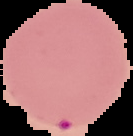
Summary:
  - Result: negative for Plasmodium parasites
  - Preparation: thin blood film
  - Image type: cell region segmented out of the field of view; surrounding area masked to black
  - Image size: 133×136 pixels